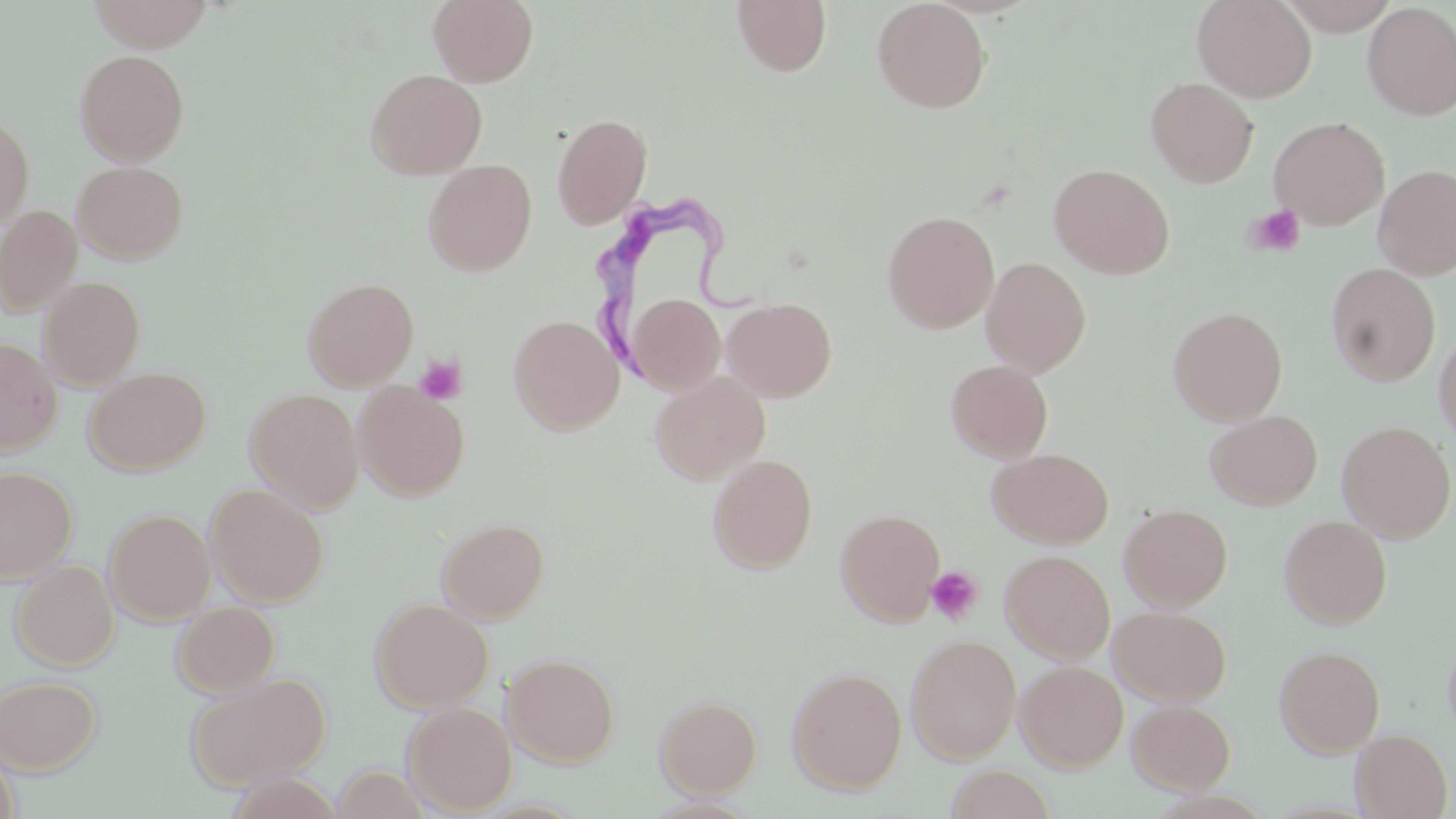
Approximate bounding boxes as (x1, y1, x2, y2) in pixels. Platelet locations: (1244, 204, 1306, 258), (414, 355, 466, 405), (926, 566, 983, 625). Uninfected red blood cell locations: (88, 0, 213, 50), (428, 0, 538, 87), (731, 0, 832, 77), (872, 0, 991, 114), (1192, 0, 1316, 103), (1276, 1, 1402, 34), (1361, 2, 1456, 121), (74, 48, 189, 165), (365, 69, 487, 179), (1145, 76, 1258, 188), (551, 112, 653, 230), (0, 114, 35, 230), (1269, 116, 1389, 229), (423, 159, 537, 277), (72, 160, 188, 264), (1048, 163, 1175, 279), (1373, 163, 1456, 280), (0, 204, 83, 317), (882, 209, 999, 333), (980, 256, 1091, 377), (1325, 263, 1440, 386), (39, 276, 145, 389), (303, 277, 419, 389), (628, 293, 725, 395), (722, 297, 837, 401), (1168, 306, 1287, 425), (508, 314, 624, 434), (1433, 328, 1456, 449), (0, 337, 61, 455), (945, 359, 1054, 463), (83, 366, 210, 475), (649, 371, 771, 484), (353, 382, 469, 500), (244, 388, 364, 512), (1206, 410, 1322, 509), (1336, 421, 1455, 542), (987, 447, 1114, 548), (707, 453, 818, 574), (0, 465, 77, 584), (205, 484, 328, 608), (1119, 503, 1233, 610), (104, 508, 216, 625), (835, 508, 946, 626), (1279, 515, 1392, 629), (436, 516, 550, 623), (1000, 549, 1115, 663), (11, 560, 119, 671), (369, 596, 494, 712), (172, 601, 280, 697), (1109, 606, 1232, 705), (1443, 632, 1456, 745), (905, 633, 1022, 763), (1275, 645, 1385, 757), (502, 653, 620, 766), (1015, 660, 1128, 771), (787, 665, 907, 795), (186, 671, 331, 791), (0, 674, 101, 774), (654, 694, 762, 797), (1127, 699, 1236, 793), (402, 702, 517, 814), (1351, 728, 1453, 819), (944, 764, 1056, 819). Trypanosoma brucei locations: (593, 202, 761, 387). Slide-level diagnosis: Trypanosoma brucei. 1000x magnification. Image is 1456×819 pixels. Single field of view. Optical microscopy. Thin blood film. May-Grünwald-Giemsa-stained preparation.